Point out each leukocyte.
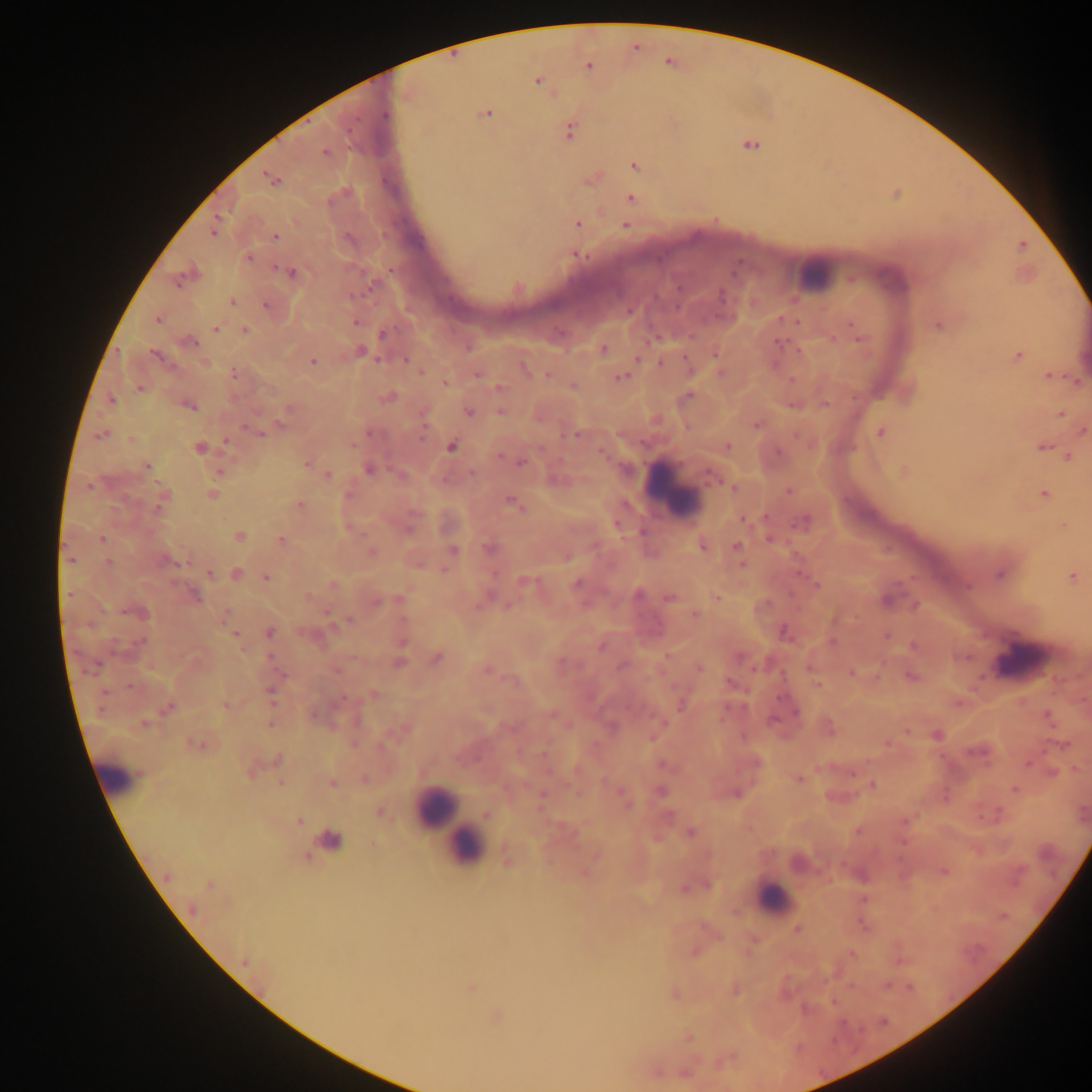

Approximate centers as [x, y] in pixels.
Leukocytes: [810, 273], [674, 487], [1017, 658], [118, 776], [437, 808], [460, 837], [466, 847], [772, 897].

Summary:
  - Malaria parasite locations: [588, 67], [538, 81], [486, 113], [385, 115], [569, 132], [751, 145], [324, 151], [634, 165], [272, 179], [631, 199], [577, 223], [626, 225], [213, 232], [275, 237], [577, 255], [248, 257], [291, 273], [178, 281], [372, 285], [352, 295], [721, 296], [232, 301], [266, 305], [158, 320], [356, 321], [854, 326], [939, 326], [215, 329], [245, 330], [383, 334], [858, 335], [189, 342], [780, 343], [468, 348], [603, 349], [360, 352], [715, 354], [157, 356], [1018, 356], [406, 360], [312, 361], [661, 363], [524, 366], [233, 373], [477, 374], [547, 375], [622, 376], [1050, 376], [792, 380], [1075, 380], [445, 382], [573, 386], [500, 388], [139, 389], [689, 395], [388, 397], [112, 400], [825, 403], [792, 405], [190, 406], [285, 411], [500, 411], [468, 412], [1061, 414], [280, 422], [757, 425], [1083, 431], [880, 432], [257, 433], [575, 435], [102, 436], [226, 442], [354, 444], [452, 446], [728, 446], [1042, 447], [199, 448], [603, 453], [500, 456], [1068, 457], [307, 463], [521, 463], [146, 465], [369, 469], [218, 471], [905, 471], [471, 472], [709, 474], [327, 475], [90, 484], [734, 487], [788, 490], [212, 494], [1044, 494], [162, 496], [513, 504], [300, 505], [159, 506], [744, 519], [803, 521], [409, 529], [239, 536], [102, 539], [770, 539], [281, 540], [736, 546], [489, 547], [702, 547], [453, 551], [371, 552], [70, 559], [168, 561], [109, 563], [209, 574], [236, 574], [999, 575], [1072, 576], [266, 577], [526, 581], [576, 584], [967, 585], [817, 586], [638, 595], [194, 596], [309, 596], [669, 598], [400, 600], [377, 602], [137, 612], [695, 615], [348, 621], [270, 632], [784, 632], [235, 635], [141, 641], [402, 641], [831, 642], [601, 647], [667, 655], [271, 657], [436, 658], [739, 658], [399, 662], [621, 666], [699, 669], [336, 670], [488, 671], [851, 673], [910, 676], [730, 683], [817, 684], [130, 687], [270, 693], [373, 695], [343, 698], [225, 705], [680, 705], [168, 707], [796, 712], [552, 716], [1048, 716], [772, 720], [144, 723], [270, 724], [937, 736], [651, 737], [196, 744], [1064, 744], [278, 759], [756, 763], [1027, 763], [663, 765], [1053, 773], [364, 779], [799, 779], [280, 783], [332, 783], [873, 785], [622, 791], [661, 791], [737, 793], [541, 795], [380, 812], [486, 814], [300, 820], [857, 832], [690, 833], [331, 839], [166, 877], [209, 885], [708, 885], [684, 888], [192, 909], [797, 928], [852, 954], [245, 962], [910, 987], [471, 988], [675, 995], [497, 1016], [689, 1038], [685, 1072]
  - Field of view: single
  - Country: Ghana
  - Preparation: thick blood smear
  - Capture: mobile-phone photograph through a microscope
  - Image size: 1092×1092 pixels